Assess this cell for malaria.
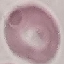
It is uninfected.

Summary:
  - Capture: smartphone camera at the microscope eyepiece
  - Preparation: thin smear
  - Image type: automatically extracted cell patch, resized to 64 × 64 pixels
  - Stain: Giemsa